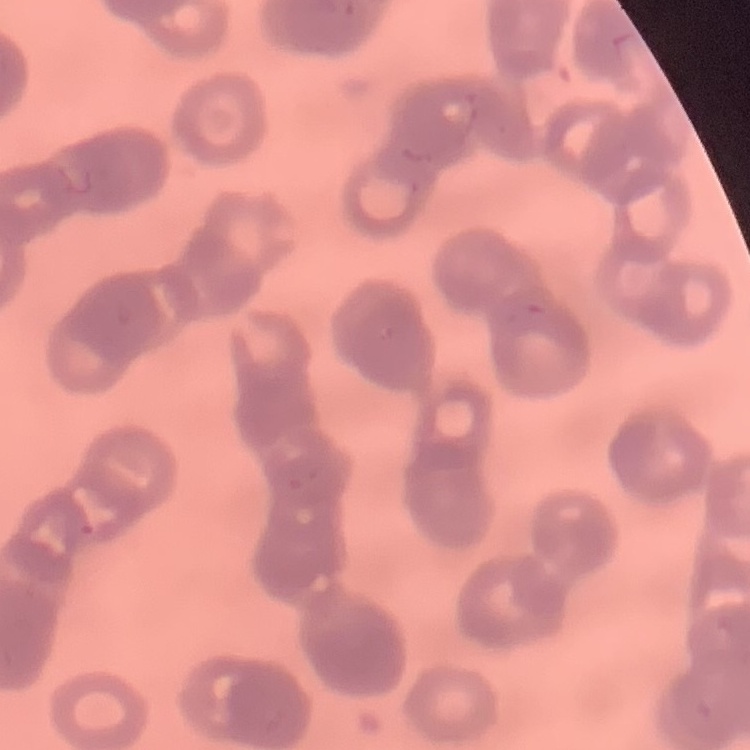

Summary:
  - Red blood cell morphology: rouleaux formation
  - Preparation: thin peripheral smear
  - Image type: square crop of a larger photomicrograph
  - Stain: Field's or Giemsa